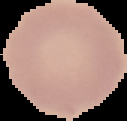
preparation = thin blood smear
image size = 127×121 pixels
malaria status = uninfected
image type = segmented cell region on a black background